Locate and identify every blood parasite.
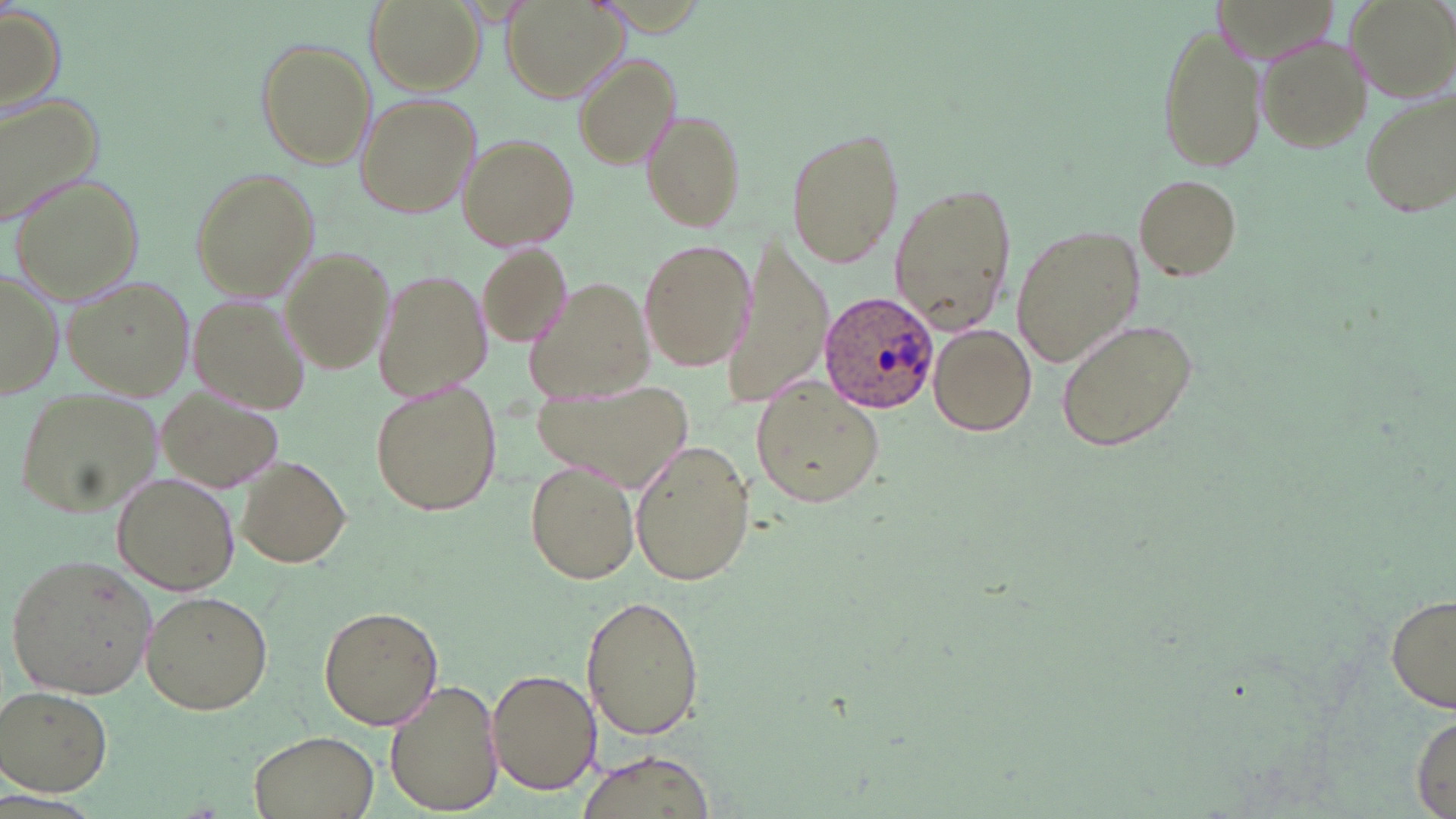

Approximate bounding boxes as named x1/y1/x2/y2 corners in pixels.
Plasmodium ovale-infected red blood cells: (x1=819, y1=289, x2=941, y2=415).
No Plasmodium falciparum, Plasmodium malariae, Plasmodium vivax, Babesia divergens, or Trypanosoma brucei observed.

Uninfected red blood cell locations: (x1=365, y1=0, x2=486, y2=96), (x1=503, y1=0, x2=630, y2=103), (x1=1349, y1=0, x2=1455, y2=101), (x1=0, y1=6, x2=68, y2=117), (x1=1153, y1=18, x2=1268, y2=174), (x1=1255, y1=35, x2=1373, y2=153), (x1=254, y1=37, x2=377, y2=170), (x1=573, y1=54, x2=681, y2=171), (x1=1356, y1=88, x2=1455, y2=222), (x1=355, y1=93, x2=480, y2=220), (x1=0, y1=94, x2=104, y2=224), (x1=640, y1=106, x2=748, y2=234), (x1=783, y1=127, x2=905, y2=268), (x1=459, y1=132, x2=581, y2=253), (x1=189, y1=166, x2=321, y2=302), (x1=10, y1=171, x2=147, y2=304), (x1=1135, y1=175, x2=1242, y2=279), (x1=889, y1=182, x2=1017, y2=335), (x1=1011, y1=224, x2=1144, y2=367), (x1=637, y1=237, x2=755, y2=370), (x1=722, y1=238, x2=833, y2=408), (x1=476, y1=241, x2=574, y2=351), (x1=281, y1=248, x2=393, y2=374), (x1=372, y1=267, x2=492, y2=403), (x1=0, y1=268, x2=63, y2=403), (x1=63, y1=274, x2=196, y2=404), (x1=527, y1=277, x2=658, y2=402), (x1=187, y1=295, x2=312, y2=417), (x1=1053, y1=313, x2=1201, y2=454), (x1=928, y1=322, x2=1038, y2=436), (x1=751, y1=378, x2=885, y2=509), (x1=372, y1=381, x2=502, y2=517), (x1=527, y1=381, x2=692, y2=488), (x1=155, y1=385, x2=286, y2=495), (x1=14, y1=386, x2=162, y2=520), (x1=629, y1=438, x2=757, y2=588), (x1=235, y1=455, x2=352, y2=569), (x1=521, y1=461, x2=639, y2=585), (x1=113, y1=472, x2=236, y2=593), (x1=6, y1=554, x2=160, y2=699), (x1=140, y1=589, x2=274, y2=718), (x1=579, y1=594, x2=708, y2=740), (x1=1386, y1=594, x2=1456, y2=716), (x1=319, y1=606, x2=443, y2=729), (x1=486, y1=668, x2=600, y2=796), (x1=383, y1=680, x2=502, y2=815), (x1=2, y1=687, x2=114, y2=796), (x1=1411, y1=713, x2=1454, y2=819), (x1=248, y1=729, x2=380, y2=819), (x1=577, y1=748, x2=717, y2=819). Slide-level diagnosis: Plasmodium ovale. Optical microscopy. Image is 1456×819 pixels. Thin blood film. May-Grünwald-Giemsa-stained preparation. Captured at 1000x magnification. Single field of view.